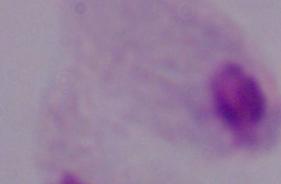

Photomicrograph. A trichomonad is seen. 1000x magnification.